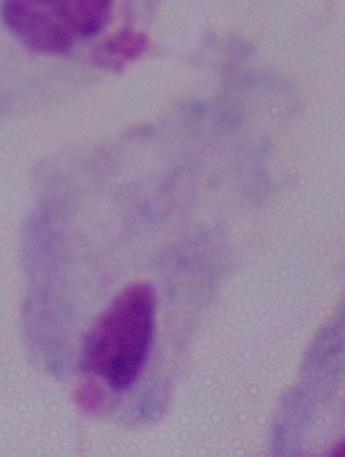 A trichomonad is shown. Micrograph. Captured at 1000x magnification.